Mark where platelets are.
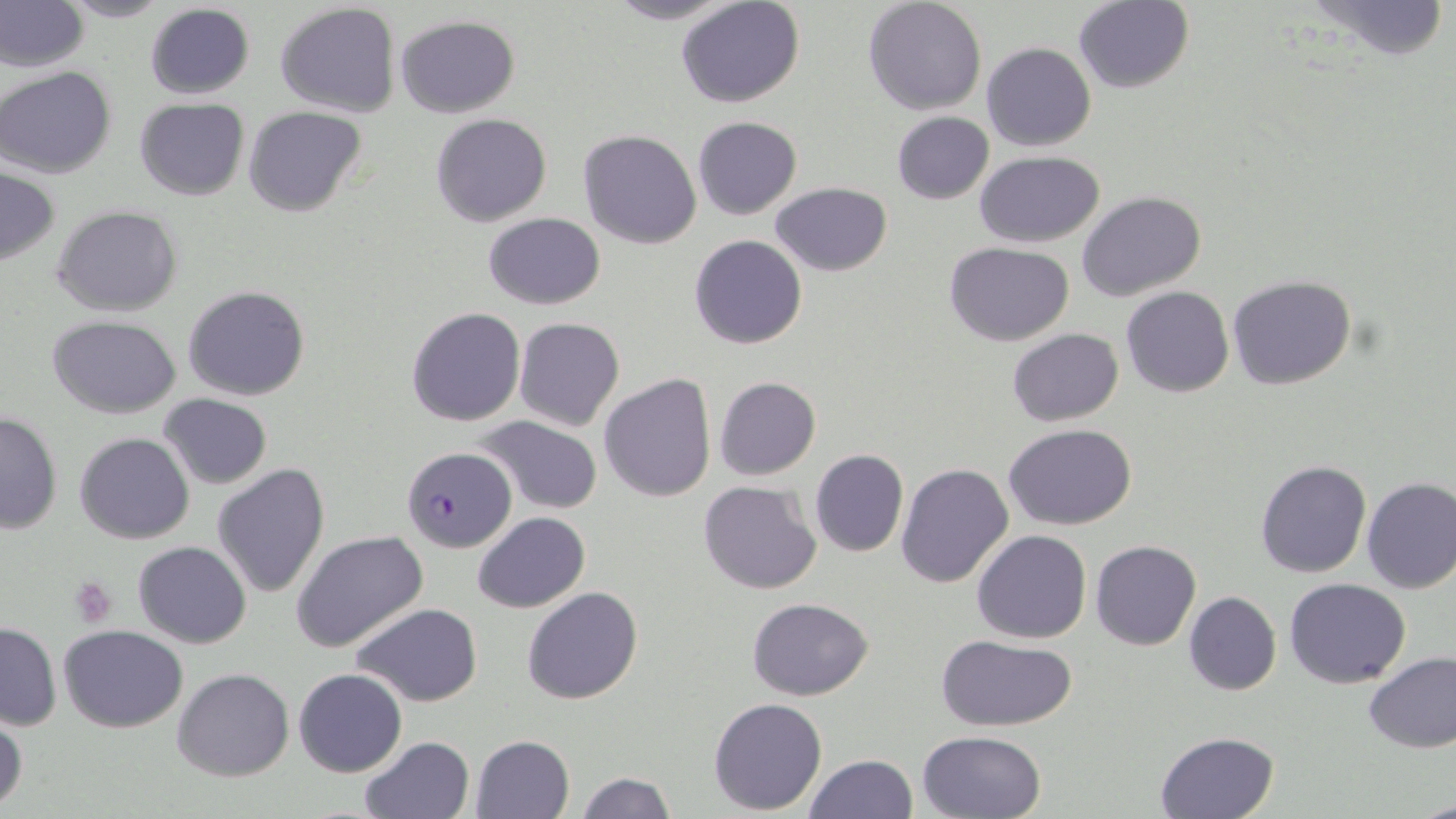

Approximate bounding boxes as (x1,y1)-(x2,y2) corner pairs in pixels.
Platelets: (70,578)-(117,629).

Plasmodium falciparum-infected red blood cell locations: (403,445)-(515,554). Uninfected red blood cell locations: (58,0)-(174,23), (601,0)-(741,24), (676,0)-(804,108), (863,0)-(986,115), (1301,0)-(1451,62), (0,2)-(86,72), (274,2)-(401,116), (1074,2)-(1195,94), (144,4)-(254,100), (394,15)-(519,118), (981,42)-(1096,151), (0,66)-(116,178), (134,99)-(249,200), (244,106)-(366,217), (892,112)-(994,205), (429,113)-(553,227), (691,117)-(802,220), (578,130)-(701,249), (975,152)-(1105,247), (1,167)-(59,265), (771,183)-(892,276), (1077,191)-(1206,302), (53,205)-(183,315), (483,212)-(605,309), (688,235)-(809,350), (944,242)-(1076,345), (1228,275)-(1356,390), (184,285)-(310,401), (1121,286)-(1234,397), (406,306)-(526,427), (48,314)-(182,417), (514,317)-(624,432), (1007,329)-(1124,426), (600,372)-(717,504), (713,376)-(821,480), (158,393)-(272,490), (0,409)-(62,535), (474,416)-(602,514), (1005,425)-(1135,530), (76,432)-(194,544), (810,449)-(908,558), (1255,460)-(1371,578), (212,462)-(330,598), (896,462)-(1013,587), (1361,476)-(1456,595), (697,480)-(823,596), (472,511)-(591,612), (971,529)-(1091,643), (291,530)-(428,653), (1090,540)-(1201,650), (133,541)-(252,648), (1285,577)-(1413,688), (521,586)-(643,705), (1184,592)-(1282,696), (748,598)-(874,700), (353,604)-(482,707), (0,620)-(61,732), (60,625)-(188,731), (936,634)-(1078,731), (1364,653)-(1456,753), (173,668)-(293,781), (293,668)-(407,777), (709,697)-(826,814), (1,711)-(27,815), (917,730)-(1046,818), (1156,731)-(1280,817), (470,734)-(575,819), (360,735)-(474,819), (804,755)-(918,818), (576,773)-(678,818), (1417,793)-(1456,819). Slide-level diagnosis: Plasmodium falciparum. Thin blood film. Optical microscopy. One field of a larger specimen. Image is 1456×819 pixels. May-Grünwald-Giemsa stain. Captured at 1000x magnification.